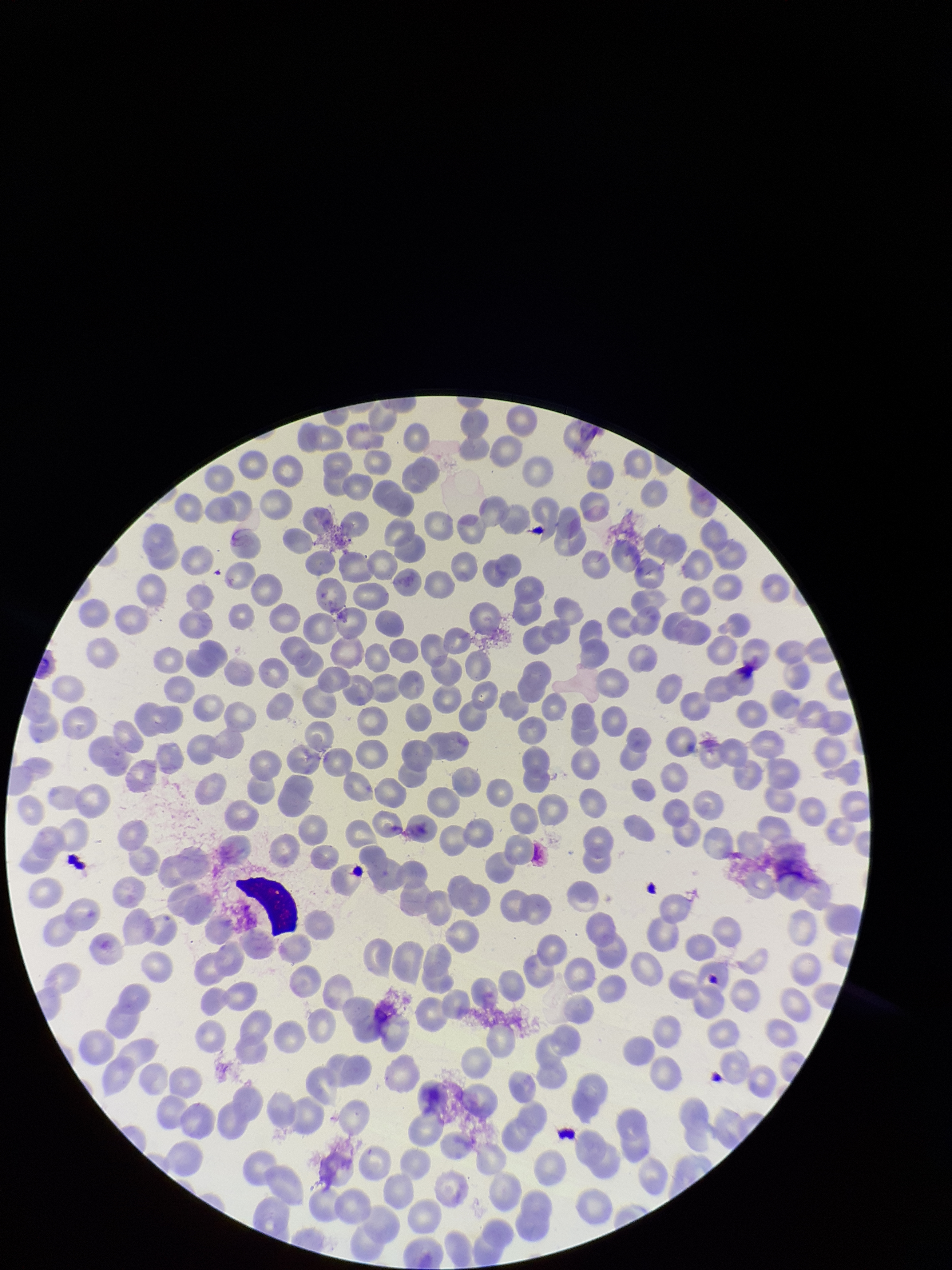
Summary:
  - Field of view: single
  - Red blood cell count: 231
  - Image size: 952×1270 pixels
  - Species reported for this patient: Plasmodium falciparum
  - Preparation: thin smear
  - Parasitized red blood cell count: 0
  - Patient malaria status: infected
  - Capture: smartphone photograph through the microscope eyepiece
  - Parasitized red blood cells: none identified
  - Stain: Giemsa